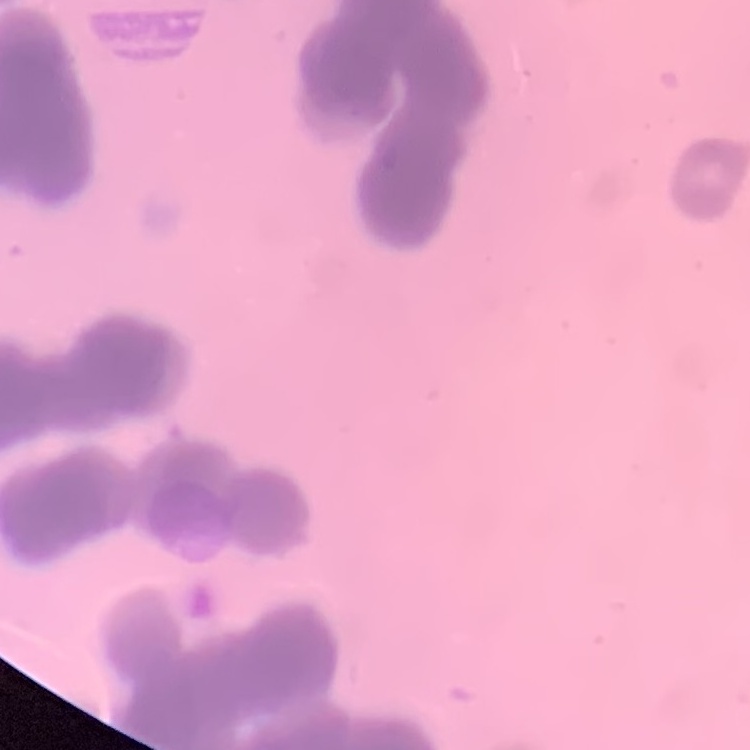 The erythrocytes show rouleaux formation. Thin blood film. Stained with either Field's or Giemsa. One tile cut from a larger photomicrograph.